Classify this cell by malaria status.
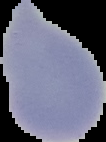
It is uninfected.

preparation = thin blood smear
image size = 106×142 pixels
image type = segmented cell region on a black background